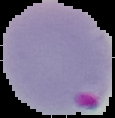
image type = segmented cell region with the area outside set to black
malaria status = parasitized
image size = 115×118 pixels
preparation = thin blood film